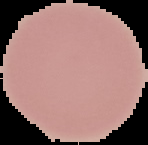

image type = cell region segmented out of the field of view; surrounding area masked to black
preparation = thin blood film
result = negative for Plasmodium parasites
image size = 148×145 pixels